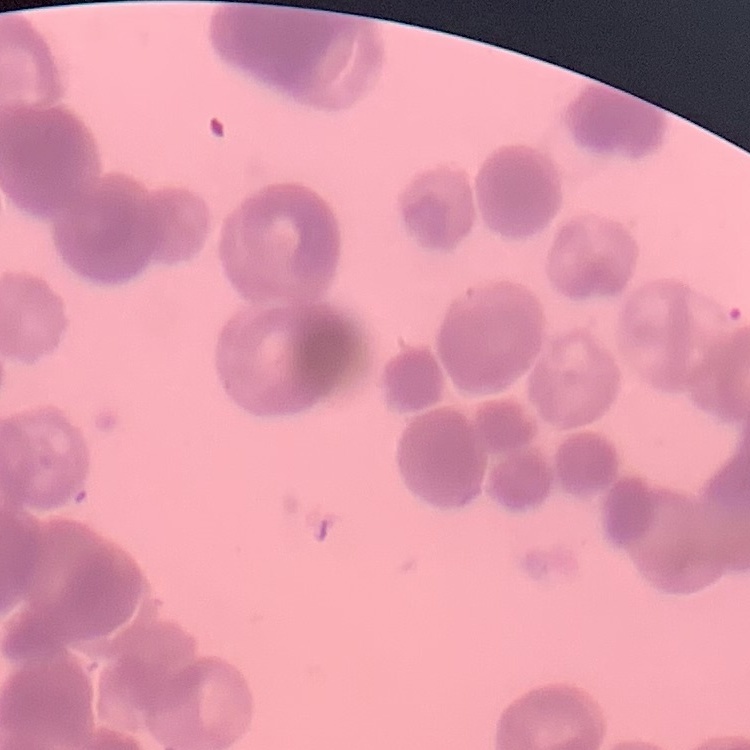
Summary:
  - Red blood cell morphology: rouleaux formation
  - Preparation: thin peripheral smear
  - Stain: Field's or Giemsa
  - Image type: one tile cut from a larger photomicrograph